Outline each white blood cell.
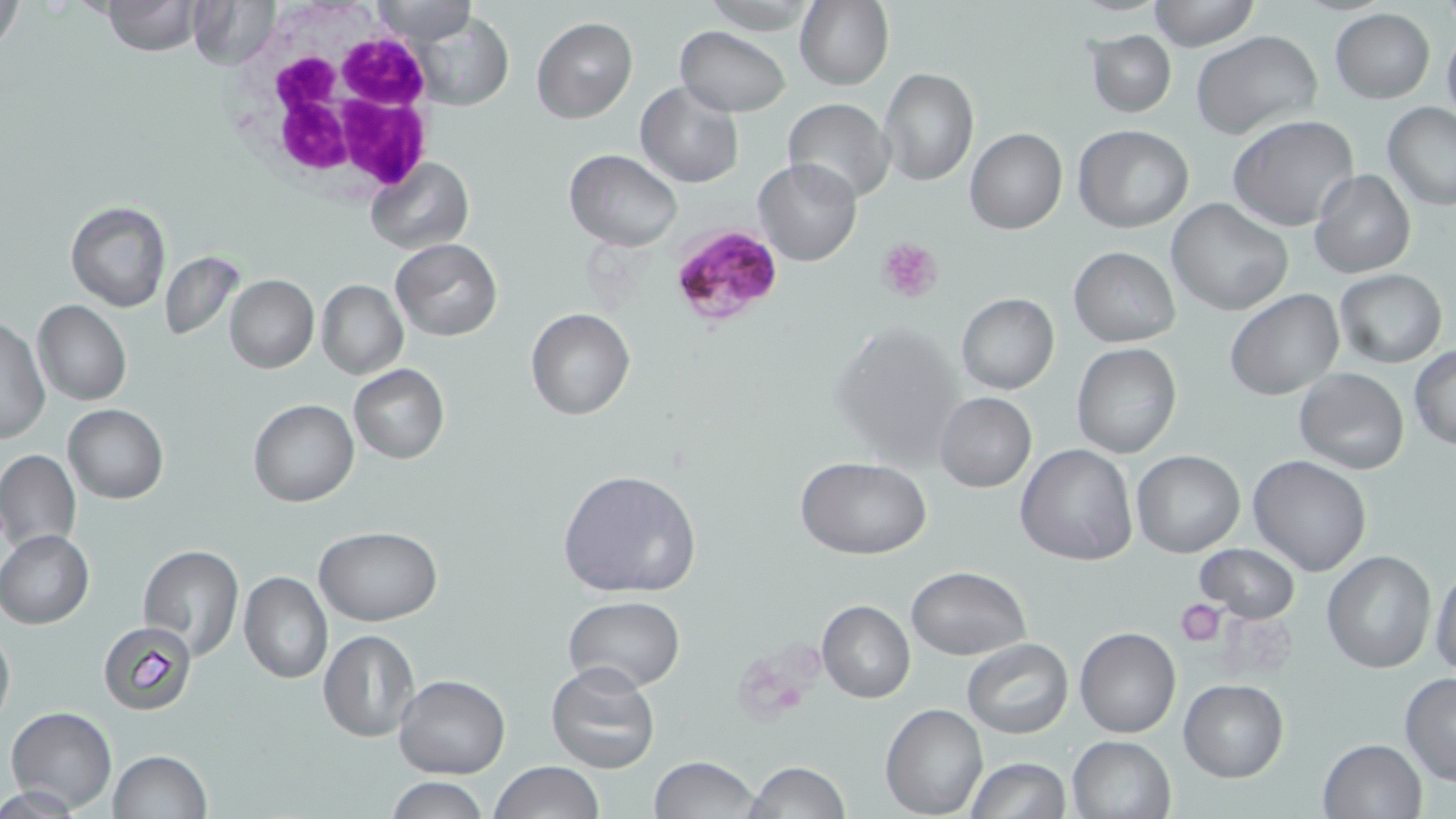
Approximate bounding boxes as (x1, y1, x2, y2) in pixels.
White blood cells: (254, 32, 437, 194).

slide_level_diagnosis: Plasmodium falciparum
stain: May-Grünwald-Giemsa
uninfected_red_blood_cell_locations: 'approximate bounding boxes as (x1, y1, x2, y2) in pixels: (0, 0, 25, 56), (101, 0, 200, 55), (187, 0, 277, 69), (795, 0, 895, 91), (365, 1, 477, 44), (1148, 1, 1258, 50), (1329, 8, 1435, 103), (410, 10, 513, 111), (532, 17, 638, 123), (1441, 24, 1456, 127), (675, 26, 790, 117), (1086, 30, 1176, 118), (1192, 31, 1323, 142), (877, 67, 980, 185), (635, 81, 744, 189), (783, 98, 896, 204), (1382, 102, 1456, 211), (1229, 114, 1359, 232), (1074, 126, 1193, 232), (965, 128, 1067, 234), (564, 149, 682, 251), (364, 155, 473, 254), (753, 157, 861, 266), (1309, 170, 1415, 278), (1166, 197, 1294, 317), (66, 202, 171, 312), (391, 239, 502, 341), (1069, 247, 1180, 346), (160, 252, 243, 340), (1333, 270, 1447, 368), (224, 275, 319, 373), (316, 279, 408, 380), (1224, 289, 1345, 402), (945, 293, 1045, 495), (955, 293, 1059, 395), (32, 300, 130, 406), (526, 308, 635, 420), (1, 317, 50, 446), (829, 321, 964, 467), (1072, 344, 1181, 459), (1408, 346, 1456, 450), (349, 364, 449, 463), (1295, 367, 1409, 476), (935, 392, 1037, 492), (248, 398, 358, 506), (63, 403, 168, 504), (1016, 443, 1139, 566), (1132, 450, 1244, 557), (0, 451, 81, 551), (795, 456, 932, 560), (1247, 456, 1373, 576), (556, 468, 702, 598), (315, 527, 442, 626), (0, 530, 93, 627), (1193, 543, 1300, 622), (138, 545, 244, 663), (1321, 550, 1436, 673), (1429, 557, 1455, 678), (905, 566, 1030, 660), (239, 572, 331, 684), (563, 595, 686, 691), (817, 600, 915, 703), (99, 620, 198, 715), (0, 622, 14, 732), (1075, 626, 1181, 738), (317, 630, 419, 742), (962, 638, 1072, 738), (546, 662, 661, 774), (1399, 673, 1456, 786), (393, 674, 510, 778), (1178, 679, 1288, 782), (881, 703, 987, 818), (6, 707, 117, 812), (1067, 735, 1177, 819), (1317, 738, 1427, 819), (108, 749, 211, 819), (649, 756, 763, 819), (967, 758, 1070, 819), (745, 761, 850, 818), (490, 762, 604, 819), (384, 777, 492, 818)'
magnification: 1000x
plasmodium_falciparum_infected_red_blood_cell_locations: 'approximate bounding boxes as (x1, y1, x2, y2) in pixels: (665, 222, 787, 329)'
field_of_view: single
modality: light microscopy
preparation: thin blood smear
platelet_locations: 'approximate bounding boxes as (x1, y1, x2, y2) in pixels: (878, 236, 945, 305), (1176, 600, 1225, 647)'
image_size: 1456×819 pixels